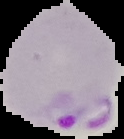
The area outside the segmented cell region is set to black. Image is 124×139 pixels. Malaria status: parasitized. From a thin blood smear.